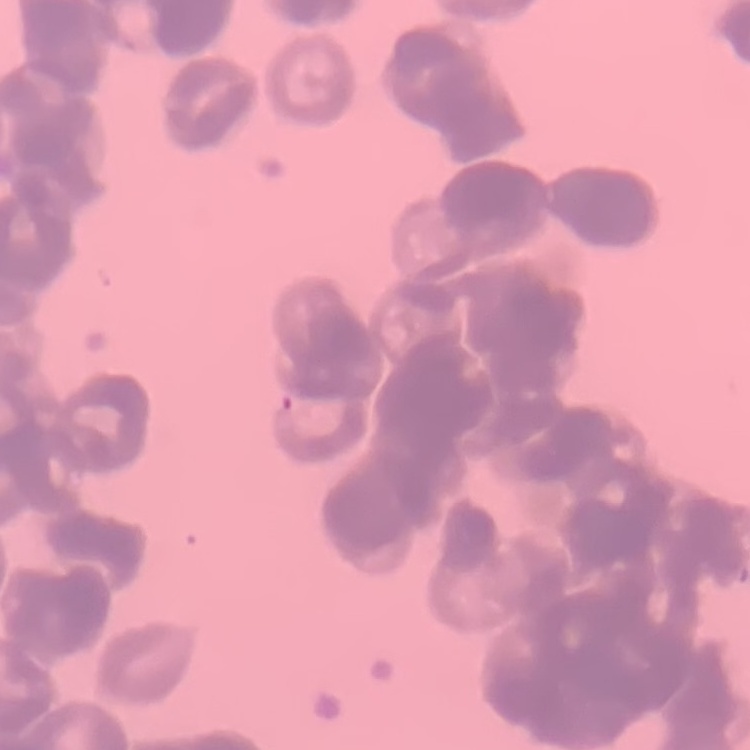

Summary:
  - Red blood cell morphology: rouleaux formation
  - Stain: Field's or Giemsa
  - Preparation: thin peripheral smear
  - Image type: square crop of a larger photomicrograph